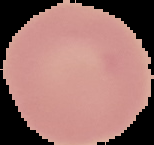
Malaria status: uninfected. Cell region segmented out of the field of view; the surrounding area is masked to black. Image is 154×145 pixels. From a thin blood film.